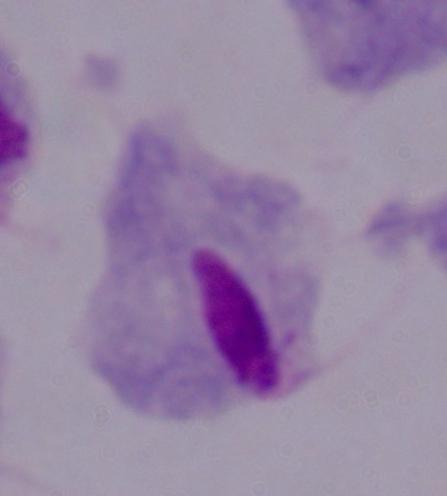
A trichomonad is seen. Micrograph. Captured at 1000x magnification.